Give the position of every Plasmodium parasite visible.
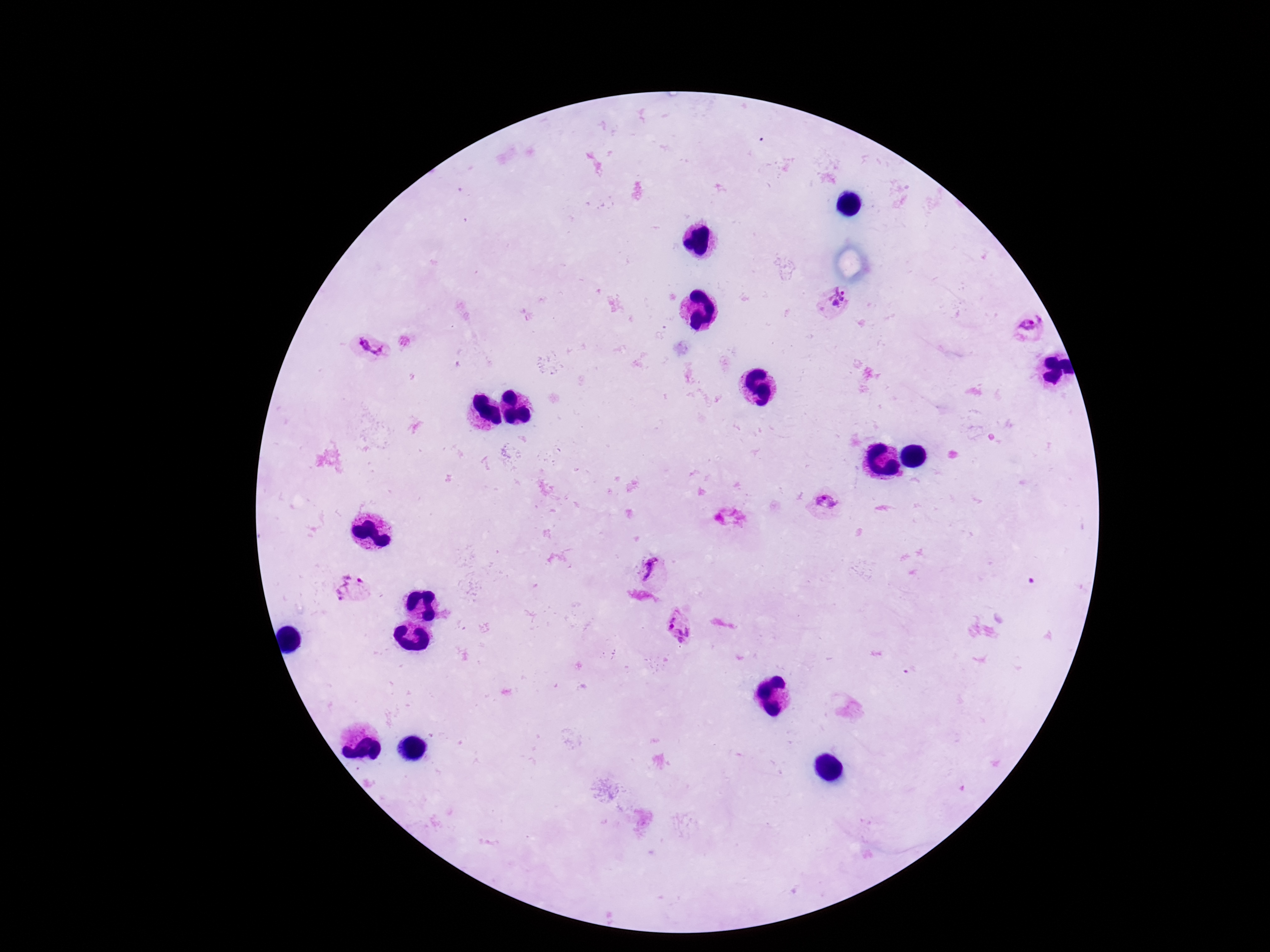

Approximate centers as [x, y] in pixels.
Plasmodium parasites: [836, 302], [1027, 329], [370, 350], [826, 502], [652, 570], [351, 591], [680, 629].

Summary:
  - Magnification: 100x
  - Stain: Giemsa
  - Image size: 1270×952 pixels
  - Preparation: thick peripheral-blood smear
  - Field of view: one from this slide
  - Patient malaria status: positive
  - Capture: smartphone camera through the microscope eyepiece